Point out each leukocyte.
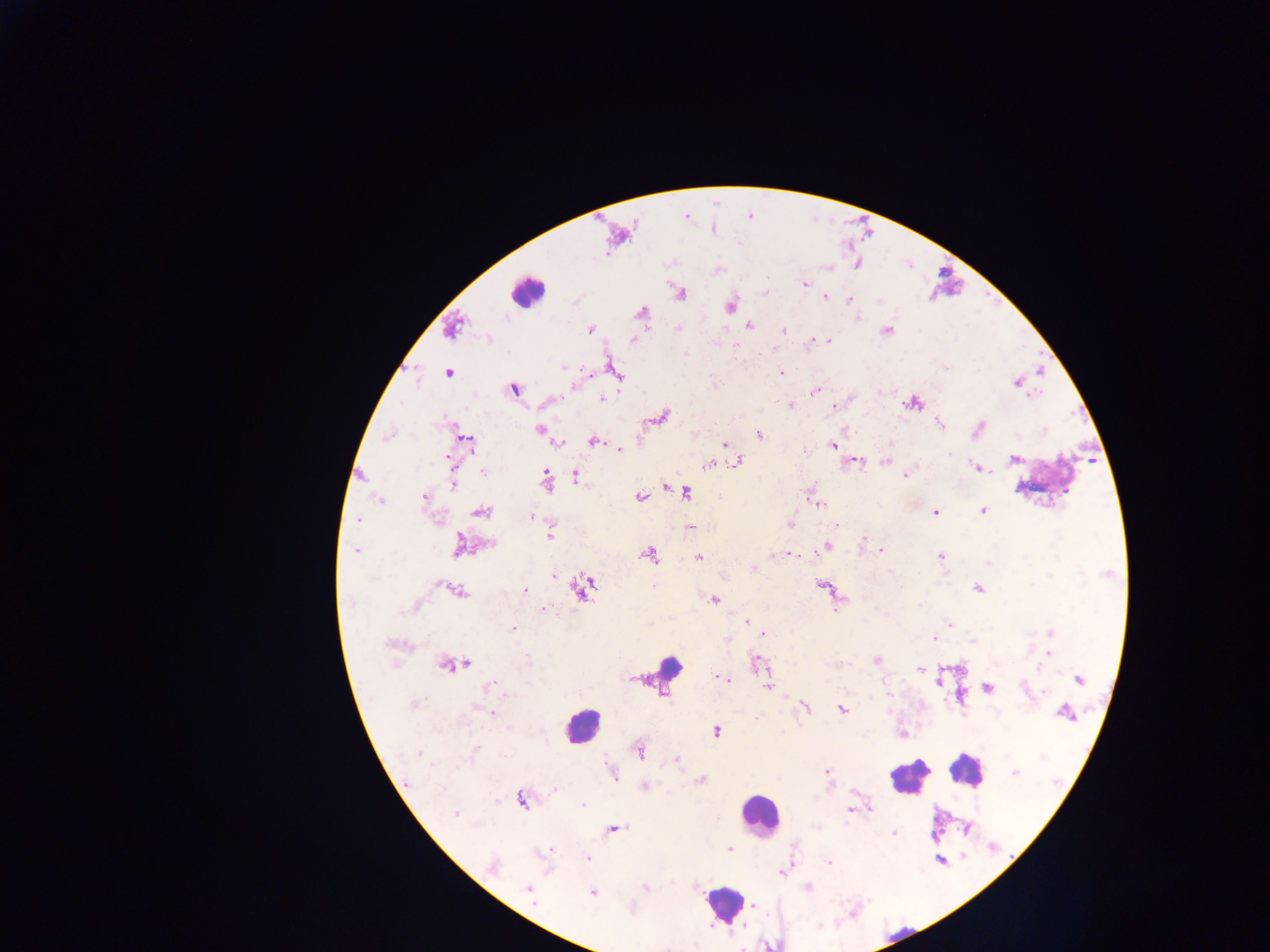

Approximate centers as x y in pixels.
Leukocytes: 527 292; 1047 479; 664 674; 582 726; 966 769; 909 776; 758 815; 724 903; 900 936; 770 943.

Plasmodium parasite locations: 687 216; 712 228; 617 234; 717 269; 804 284; 680 292; 824 297; 849 299; 731 305; 641 312; 748 324; 452 327; 589 329; 886 330; 781 331; 632 339; 811 340; 828 340; 615 372; 781 372; 448 373; 1017 382; 575 385; 514 389; 817 390; 602 400; 549 402; 913 402; 790 405; 834 407; 662 416; 940 424; 539 429; 977 429; 758 433; 387 436; 465 440; 593 441; 558 442; 724 444; 833 445; 619 449; 1013 459; 738 461; 854 461; 885 462; 709 463; 977 467; 482 470; 905 473; 575 476; 545 479; 453 480; 666 485; 685 492; 639 497; 814 497; 424 498; 379 500; 817 503; 983 510; 481 511; 936 512; 532 516; 358 519; 789 524; 838 526; 690 527; 549 534; 863 539; 490 544; 458 545; 826 545; 356 550; 879 550; 648 554; 789 554; 941 556; 698 557; 754 569; 553 576; 654 585; 822 585; 582 587; 977 588; 455 589; 525 590; 713 599; 544 609; 747 620; 949 623; 512 628; 1050 632; 763 633; 933 639; 727 640; 394 644; 1048 654; 876 660; 450 664; 757 664; 920 669; 631 678; 722 678; 1078 679; 768 686; 987 687; 488 688; 1044 693; 804 707; 841 709; 492 712; 1065 712; 716 731; 901 733; 476 749; 638 750; 419 753; 676 760; 827 772; 1014 772; 611 773; 699 780; 645 786; 554 788; 521 798; 582 805; 851 809; 456 814; 613 828; 966 829; 894 832; 729 849; 548 851; 588 858; 940 859; 829 862; 493 867; 784 872; 646 887; 806 888; 529 889; 591 892; 754 906. One field of view. Image is 1270×952 pixels. Thick blood smear. Mobile-phone photograph taken through the microscope. Sample from Ghana.